Locate every malaria parasite by life-cycle stage, and every leukocyte.
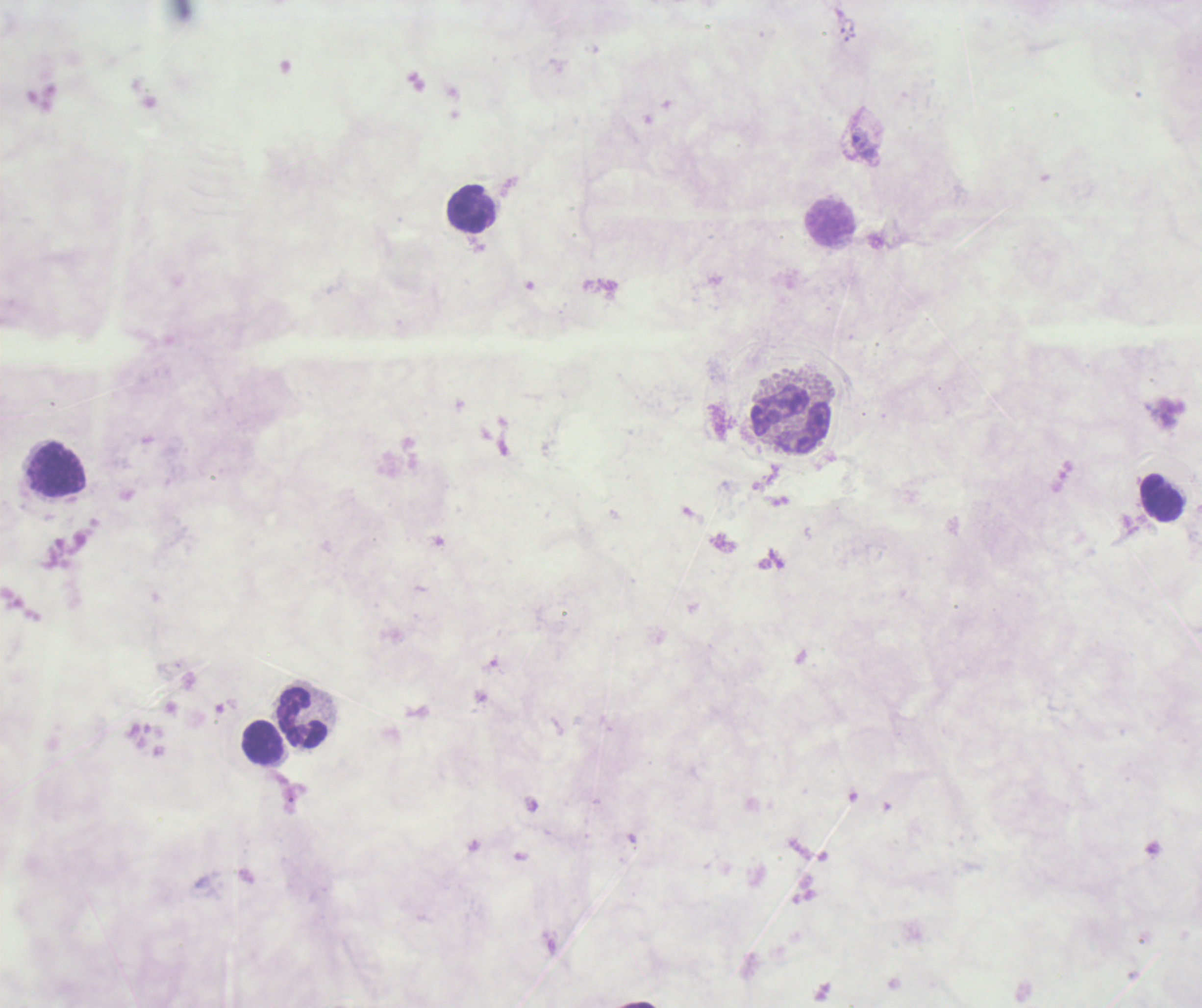
Negative for malaria parasites.
Approximate centers as (x, y) in pixels.
Leukocytes: (472, 209), (830, 224), (790, 420), (56, 470), (1162, 498), (303, 717), (262, 742).

Romanowsky stain. One field from this slide. Image is 1202×1008 pixels. Previously used in a real diagnosis. Coloration quality: bad. 100x magnification. Background quality: unsatisfactory. Thick blood film.